Name the parasite shown.
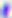

Toxoplasma gondii.

400x magnification. Micrograph.